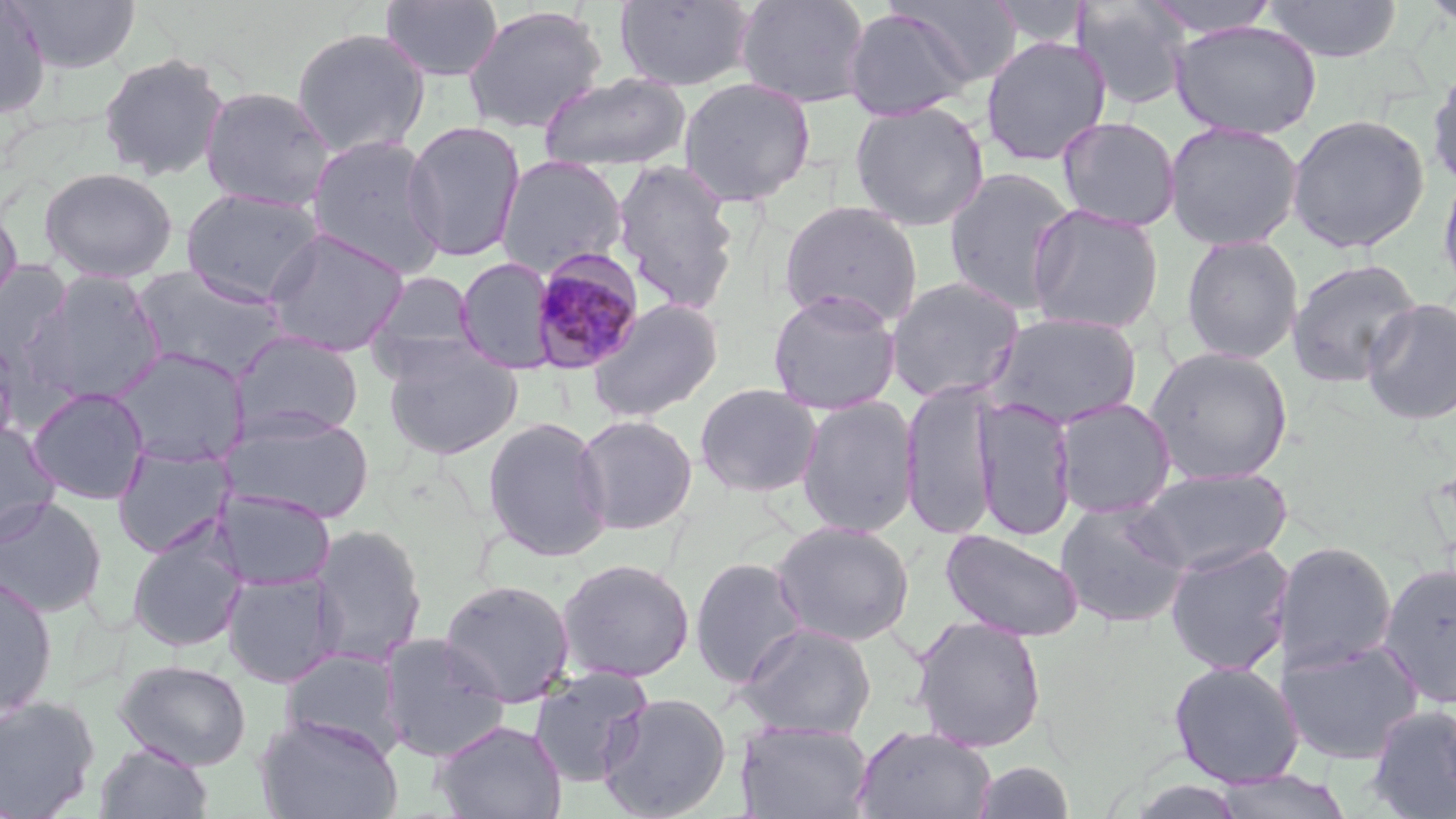
{
  "plasmodium_malariae_infected_red_blood_cell_locations": "approximate bounding boxes as named x1/y1/x2/y2 corners in pixels: (x1=529, y1=248, x2=646, y2=375)",
  "slide_level_diagnosis": "Plasmodium malariae",
  "preparation": "thin blood smear",
  "stain": "May-Grünwald-Giemsa",
  "magnification": "1000x",
  "uninfected_red_blood_cell_locations": "approximate bounding boxes as named x1/y1/x2/y2 corners in pixels: (x1=8, y1=0, x2=142, y2=74), (x1=613, y1=0, x2=757, y2=92), (x1=734, y1=0, x2=873, y2=109), (x1=888, y1=0, x2=1024, y2=88), (x1=1072, y1=0, x2=1193, y2=111), (x1=1144, y1=0, x2=1281, y2=39), (x1=1261, y1=0, x2=1403, y2=63), (x1=1417, y1=0, x2=1456, y2=31), (x1=0, y1=1, x2=52, y2=119), (x1=379, y1=1, x2=504, y2=82), (x1=987, y1=1, x2=1090, y2=50), (x1=461, y1=4, x2=607, y2=135), (x1=843, y1=7, x2=976, y2=121), (x1=1169, y1=20, x2=1322, y2=141), (x1=291, y1=26, x2=431, y2=159), (x1=980, y1=35, x2=1112, y2=166), (x1=97, y1=51, x2=231, y2=182), (x1=1426, y1=65, x2=1456, y2=191), (x1=538, y1=71, x2=692, y2=173), (x1=677, y1=76, x2=816, y2=206), (x1=200, y1=86, x2=335, y2=212), (x1=849, y1=100, x2=990, y2=231), (x1=1286, y1=113, x2=1431, y2=254), (x1=1056, y1=116, x2=1181, y2=232), (x1=1165, y1=120, x2=1303, y2=251), (x1=402, y1=121, x2=525, y2=262), (x1=305, y1=133, x2=448, y2=279), (x1=495, y1=155, x2=629, y2=278), (x1=610, y1=158, x2=742, y2=316), (x1=1437, y1=165, x2=1456, y2=298), (x1=39, y1=166, x2=178, y2=283), (x1=944, y1=166, x2=1078, y2=315), (x1=181, y1=188, x2=325, y2=305), (x1=779, y1=200, x2=923, y2=330), (x1=1026, y1=203, x2=1165, y2=335), (x1=0, y1=204, x2=23, y2=315), (x1=262, y1=226, x2=410, y2=357), (x1=1180, y1=234, x2=1303, y2=364), (x1=456, y1=257, x2=557, y2=374), (x1=1287, y1=257, x2=1423, y2=388), (x1=0, y1=262, x2=73, y2=362), (x1=131, y1=264, x2=289, y2=380), (x1=23, y1=271, x2=168, y2=406), (x1=366, y1=271, x2=481, y2=375), (x1=885, y1=276, x2=1025, y2=405), (x1=767, y1=290, x2=902, y2=415), (x1=1361, y1=298, x2=1456, y2=426), (x1=587, y1=299, x2=723, y2=422), (x1=985, y1=311, x2=1144, y2=430), (x1=232, y1=330, x2=364, y2=441), (x1=0, y1=338, x2=28, y2=450), (x1=383, y1=342, x2=522, y2=460), (x1=1144, y1=346, x2=1294, y2=486), (x1=109, y1=348, x2=248, y2=468), (x1=900, y1=378, x2=1002, y2=542), (x1=694, y1=383, x2=822, y2=498), (x1=27, y1=387, x2=150, y2=504), (x1=797, y1=395, x2=919, y2=537), (x1=974, y1=396, x2=1077, y2=541), (x1=1053, y1=398, x2=1176, y2=519), (x1=226, y1=409, x2=376, y2=525), (x1=573, y1=414, x2=698, y2=535), (x1=482, y1=415, x2=613, y2=562), (x1=0, y1=423, x2=60, y2=544), (x1=113, y1=442, x2=234, y2=558), (x1=1131, y1=466, x2=1293, y2=577), (x1=214, y1=489, x2=336, y2=592), (x1=0, y1=496, x2=108, y2=619), (x1=1055, y1=499, x2=1190, y2=628), (x1=771, y1=520, x2=915, y2=647), (x1=127, y1=522, x2=247, y2=654), (x1=309, y1=524, x2=428, y2=666), (x1=940, y1=528, x2=1086, y2=643), (x1=1275, y1=540, x2=1397, y2=675), (x1=1164, y1=541, x2=1295, y2=675), (x1=689, y1=557, x2=809, y2=688), (x1=556, y1=558, x2=695, y2=683), (x1=1377, y1=562, x2=1456, y2=709), (x1=222, y1=570, x2=342, y2=688), (x1=0, y1=572, x2=59, y2=722), (x1=438, y1=578, x2=575, y2=707), (x1=910, y1=615, x2=1047, y2=753), (x1=737, y1=622, x2=877, y2=739), (x1=379, y1=633, x2=510, y2=762), (x1=1280, y1=637, x2=1424, y2=764), (x1=279, y1=648, x2=404, y2=757), (x1=114, y1=658, x2=252, y2=771), (x1=1167, y1=659, x2=1304, y2=788), (x1=527, y1=667, x2=654, y2=788), (x1=598, y1=692, x2=732, y2=819), (x1=0, y1=695, x2=100, y2=818), (x1=1365, y1=703, x2=1456, y2=818), (x1=255, y1=714, x2=404, y2=819), (x1=433, y1=718, x2=567, y2=819), (x1=736, y1=721, x2=874, y2=819), (x1=853, y1=724, x2=997, y2=819), (x1=94, y1=742, x2=213, y2=819), (x1=972, y1=760, x2=1076, y2=819), (x1=1212, y1=769, x2=1355, y2=818)",
  "field_of_view": "single",
  "image_size": "1456×819 pixels",
  "modality": "optical microscopy"
}